Give the position of every Plasmodium parasite.
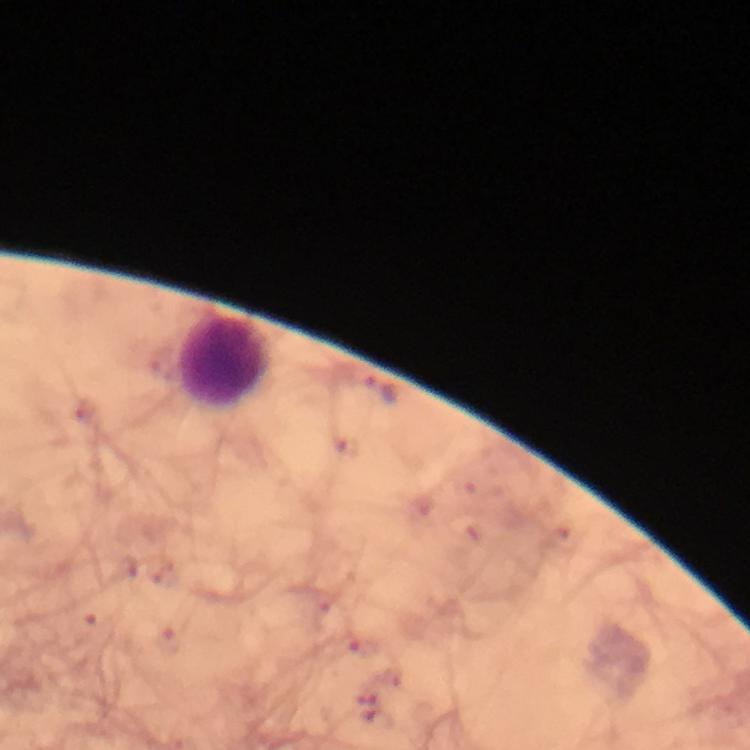
Approximate centers as {x, y} in pixels.
Plasmodium parasites: {381, 389}, {96, 623}, {168, 641}, {366, 650}.

Leukocyte locations: {226, 362}. A crop from one field of view. From a diagnostic examination for malaria. Thick blood smear. Image is 750×750 pixels. Immersion oil applied. 100x magnification. Giemsa stain. Photographed through the microscope with a smartphone camera.